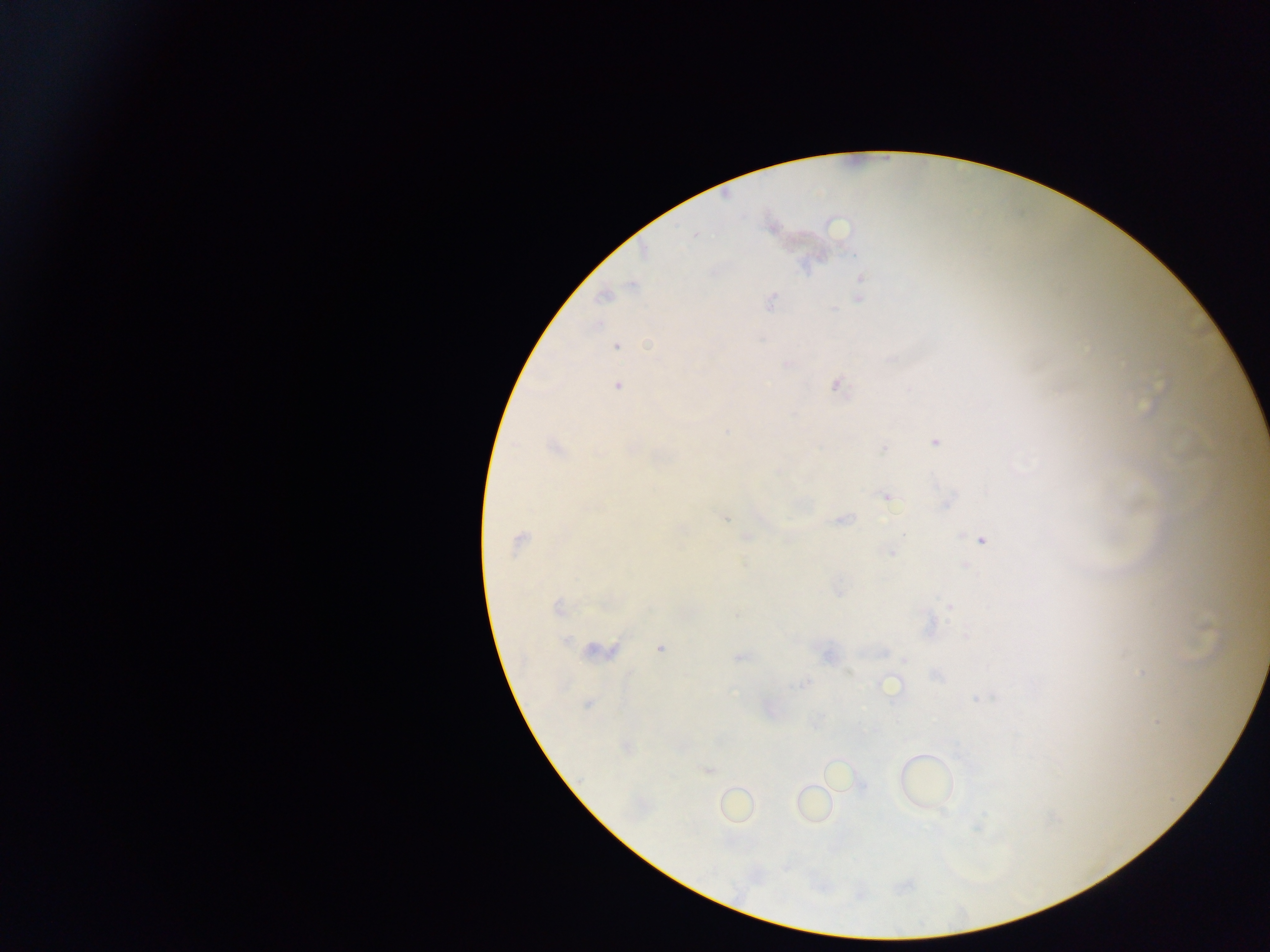

Approximate centers as x y in pixels.
Summary:
  - Malaria parasite locations: 695 235; 861 281; 631 285; 603 296; 859 298; 770 301; 617 347; 788 364; 617 386; 837 386; 934 442; 554 447; 633 449; 884 449; 886 497; 724 517; 843 519; 746 537; 981 540; 518 541; 891 552; 963 566; 558 608; 950 608; 1206 628; 965 635; 566 640; 597 649; 660 649; 884 653; 827 656; 740 657; 1142 674; 805 683; 890 685; 977 699; 588 704; 1157 722; 626 748; 708 770
  - Image size: 1270×952 pixels
  - Preparation: thick blood film
  - Capture: mobile-phone photograph through a microscope
  - Country: Ghana
  - Field of view: single